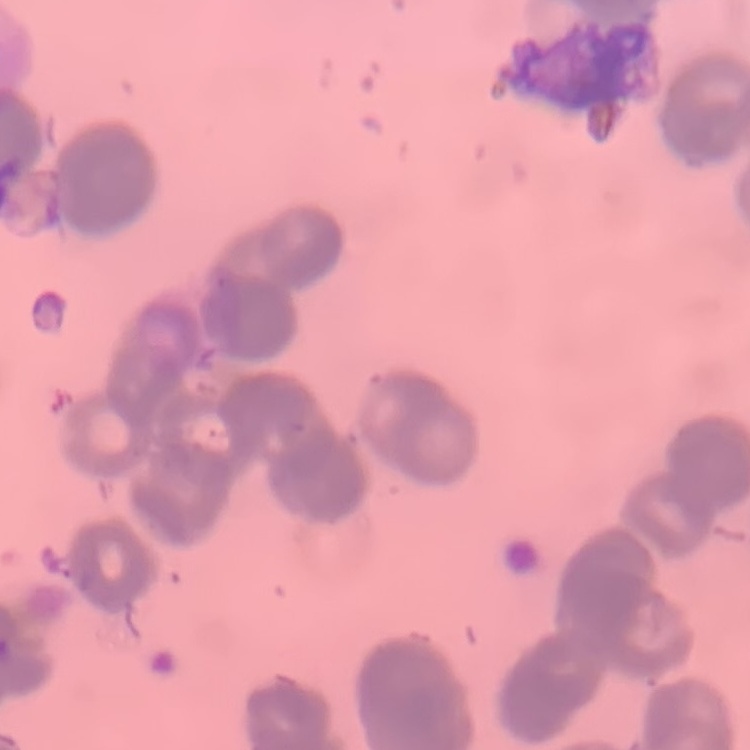
erythrocyte morphology = rouleaux formation
stain = Field's or Giemsa
image type = one tile cut from a larger photomicrograph
preparation = thin blood film